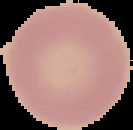

Summary:
  - Preparation: thin blood smear
  - Malaria status: uninfected
  - Image type: segmented cell region with the area outside set to black
  - Image size: 133×130 pixels